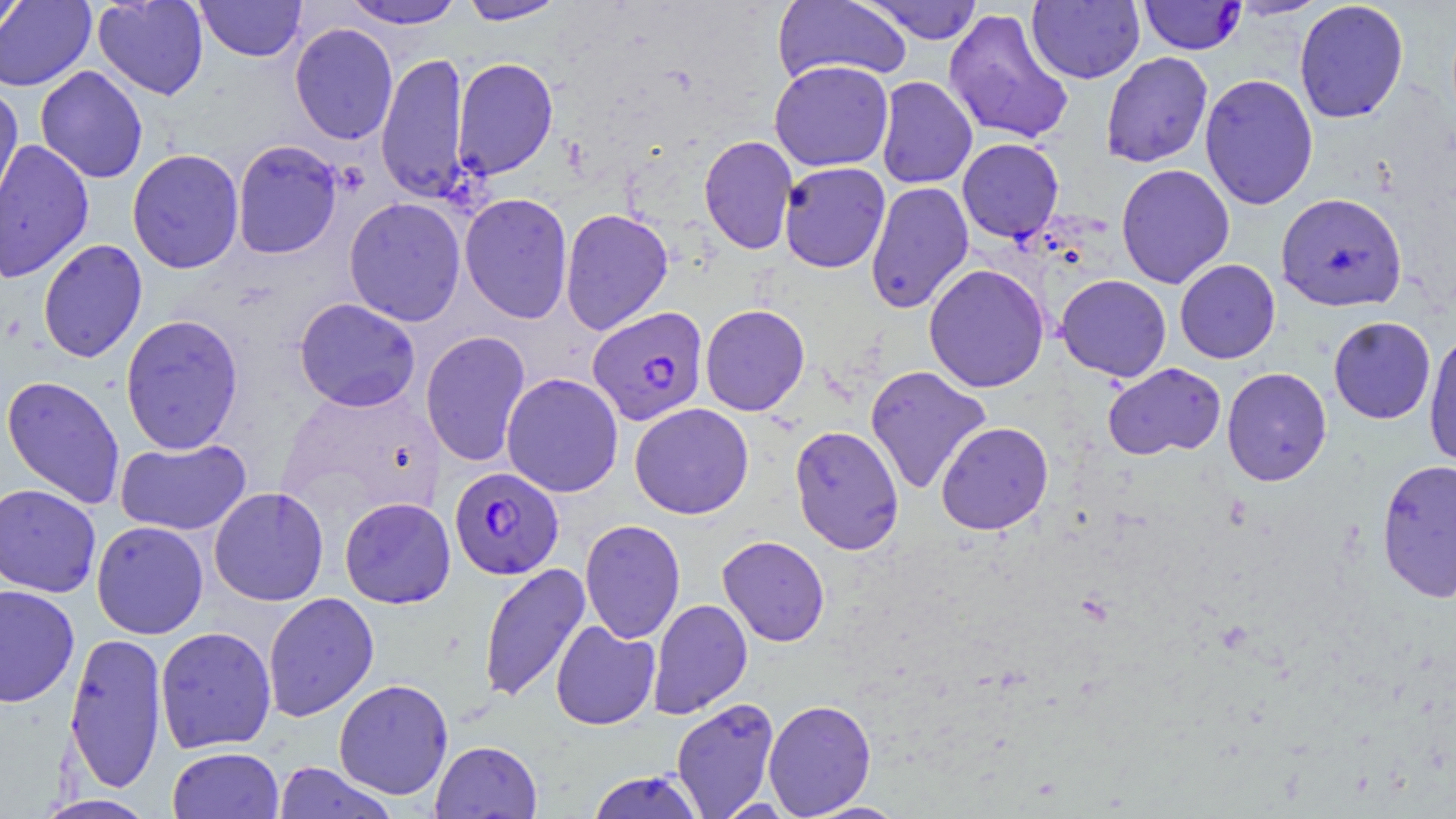
slide_level_diagnosis: Plasmodium falciparum
magnification: 1000x
preparation: thin blood film
modality: light microscopy
plasmodium_falciparum_infected_red_blood_cell_locations: 'approximate bounding boxes as [x1, y1, x2, y2] in pixels: [1137, 0, 1246, 55], [1276, 192, 1407, 312], [587, 306, 709, 425], [448, 467, 564, 580]'
field_of_view: single
uninfected_red_blood_cell_locations: 'approximate bounding boxes as [x1, y1, x2, y2] in pixels: [92, 0, 209, 100], [341, 0, 466, 29], [458, 0, 568, 25], [772, 0, 911, 85], [861, 0, 984, 44], [1227, 0, 1329, 19], [0, 1, 96, 92], [0, 1, 30, 43], [195, 1, 307, 62], [1027, 1, 1144, 84], [1294, 1, 1409, 124], [943, 8, 1074, 145], [290, 22, 398, 145], [376, 51, 470, 203], [1100, 51, 1214, 168], [452, 57, 559, 180], [769, 60, 894, 171], [35, 66, 149, 183], [1199, 73, 1319, 210], [875, 76, 977, 189], [0, 86, 24, 221], [699, 134, 798, 254], [957, 138, 1064, 243], [0, 139, 94, 283], [231, 140, 343, 259], [127, 149, 244, 274], [778, 162, 891, 273], [1115, 163, 1235, 288], [865, 181, 974, 314], [459, 192, 574, 324], [343, 197, 467, 326], [559, 208, 673, 335], [38, 239, 147, 363], [1175, 259, 1280, 363], [923, 264, 1050, 393], [1056, 274, 1172, 382], [294, 297, 421, 412], [700, 304, 810, 416], [120, 314, 244, 455], [1328, 316, 1436, 423], [1423, 329, 1456, 470], [420, 331, 531, 468], [1102, 362, 1226, 460], [865, 365, 992, 495], [1222, 367, 1332, 486], [501, 372, 624, 498], [1, 375, 125, 509], [896, 394, 1030, 521], [629, 403, 754, 519], [936, 421, 1053, 535], [789, 424, 905, 555], [115, 438, 251, 535], [1376, 458, 1456, 602], [0, 484, 102, 598], [208, 487, 329, 606], [339, 497, 455, 608], [580, 519, 685, 644], [91, 521, 208, 639], [717, 535, 830, 646], [478, 562, 590, 704], [0, 585, 80, 707], [262, 591, 379, 722], [648, 598, 752, 719], [550, 620, 661, 730], [155, 626, 276, 753], [64, 631, 167, 794], [333, 678, 454, 801], [671, 697, 780, 819], [763, 698, 877, 817], [430, 740, 542, 818], [167, 746, 284, 819], [272, 762, 398, 818], [586, 770, 705, 819], [32, 794, 159, 818], [802, 800, 908, 818]'
image_size: 1456×819 pixels
stain: May-Grünwald-Giemsa